State which parasite is depicted.
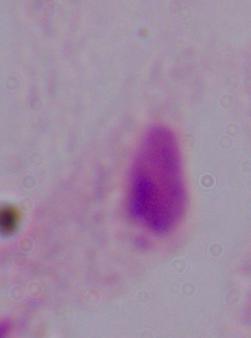
A trichomonad.

1000x magnification. Photomicrograph.